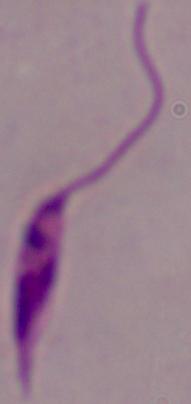

Summary:
  - Magnification: 1000x
  - Identification: Leishmania
  - Modality: photomicrograph